Assess this cell for malaria.
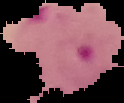
It is parasitized.

From a thin blood smear. Image is 124×103 pixels. Segmented cell region on a black background.